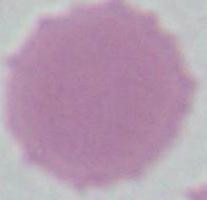

identification: red blood cell
modality: photomicrograph
magnification: 1000x